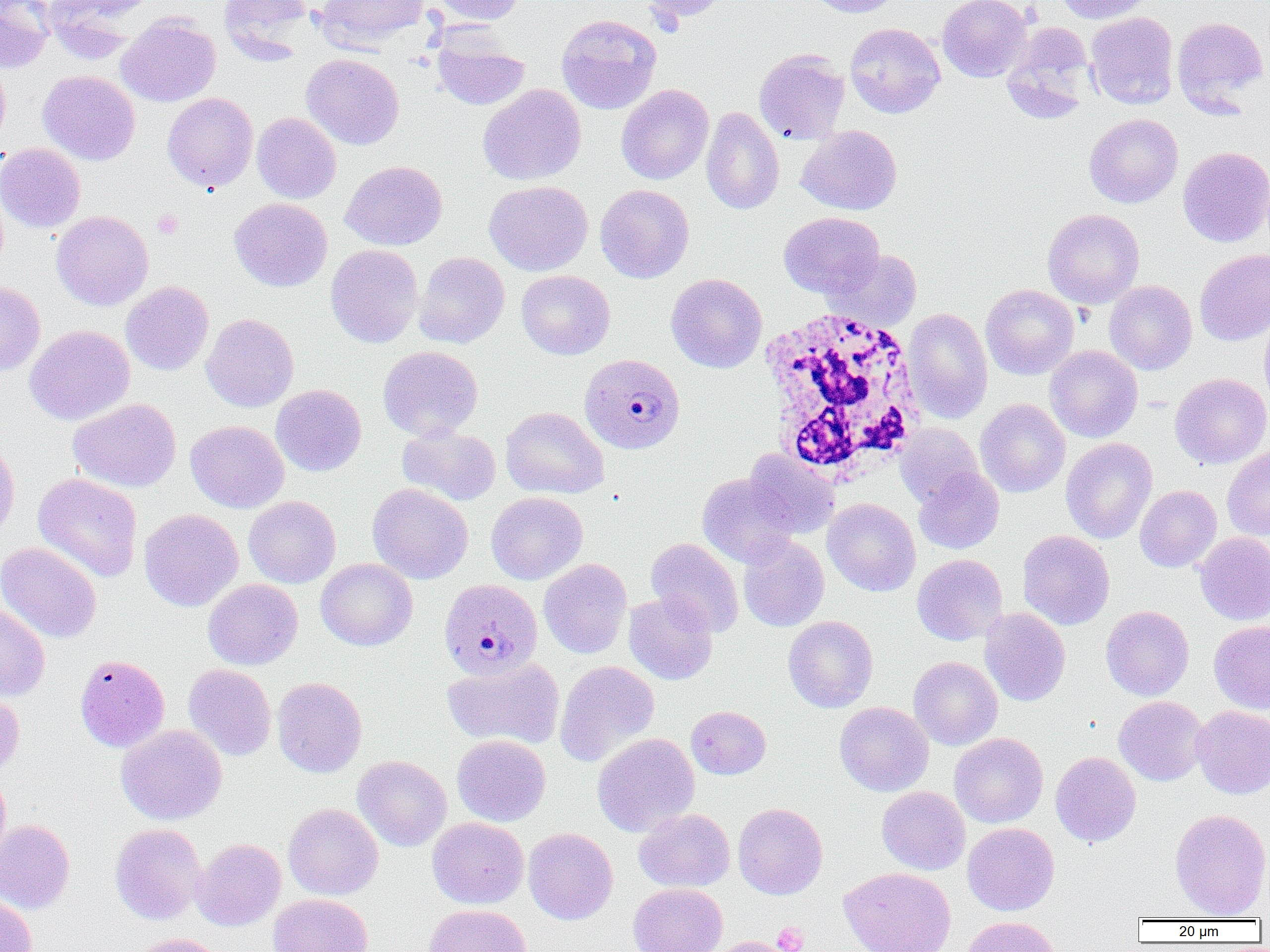
Summary:
  - Coordinate format: approximate bounding boxes as named x1/y1/x2/y2 corners in pixels
  - White blood cell locations: (x1=757, y1=308, x2=928, y2=479)
  - Plasmodium malariae-infected red blood cell locations: (x1=580, y1=353, x2=686, y2=455), (x1=441, y1=583, x2=544, y2=684)
  - Uninfected red blood cell locations: (x1=0, y1=0, x2=55, y2=73), (x1=42, y1=0, x2=148, y2=62), (x1=219, y1=0, x2=312, y2=62), (x1=314, y1=0, x2=428, y2=52), (x1=431, y1=0, x2=526, y2=25), (x1=641, y1=0, x2=730, y2=24), (x1=806, y1=0, x2=902, y2=17), (x1=937, y1=0, x2=1032, y2=82), (x1=1055, y1=0, x2=1151, y2=24), (x1=1085, y1=12, x2=1178, y2=109), (x1=556, y1=13, x2=662, y2=114), (x1=116, y1=14, x2=220, y2=107), (x1=1172, y1=16, x2=1268, y2=112), (x1=844, y1=23, x2=945, y2=118), (x1=1002, y1=23, x2=1095, y2=123), (x1=432, y1=31, x2=529, y2=110), (x1=754, y1=49, x2=850, y2=144), (x1=301, y1=53, x2=404, y2=150), (x1=0, y1=56, x2=11, y2=149), (x1=37, y1=70, x2=140, y2=165), (x1=478, y1=84, x2=586, y2=186), (x1=616, y1=84, x2=714, y2=184), (x1=162, y1=93, x2=258, y2=191), (x1=701, y1=106, x2=784, y2=215), (x1=252, y1=112, x2=341, y2=204), (x1=1084, y1=113, x2=1183, y2=207), (x1=796, y1=125, x2=902, y2=215), (x1=0, y1=143, x2=86, y2=232), (x1=1178, y1=146, x2=1270, y2=247), (x1=340, y1=160, x2=447, y2=250), (x1=484, y1=180, x2=593, y2=276), (x1=595, y1=184, x2=694, y2=283), (x1=229, y1=198, x2=332, y2=291), (x1=1043, y1=208, x2=1144, y2=308), (x1=52, y1=211, x2=153, y2=310), (x1=778, y1=211, x2=884, y2=297), (x1=326, y1=244, x2=423, y2=347), (x1=1195, y1=248, x2=1270, y2=346), (x1=825, y1=249, x2=923, y2=330), (x1=413, y1=252, x2=509, y2=348), (x1=516, y1=270, x2=615, y2=360), (x1=666, y1=273, x2=767, y2=373), (x1=0, y1=280, x2=46, y2=376), (x1=1104, y1=280, x2=1197, y2=375), (x1=121, y1=281, x2=214, y2=375), (x1=981, y1=285, x2=1078, y2=379), (x1=903, y1=308, x2=993, y2=423), (x1=1259, y1=312, x2=1270, y2=410), (x1=201, y1=313, x2=299, y2=412), (x1=25, y1=325, x2=135, y2=425), (x1=378, y1=345, x2=483, y2=440), (x1=1045, y1=345, x2=1143, y2=442), (x1=1169, y1=373, x2=1270, y2=468), (x1=271, y1=384, x2=366, y2=476), (x1=68, y1=398, x2=181, y2=492), (x1=974, y1=399, x2=1070, y2=497), (x1=501, y1=406, x2=608, y2=499), (x1=185, y1=420, x2=289, y2=513), (x1=397, y1=423, x2=501, y2=505), (x1=895, y1=423, x2=983, y2=507), (x1=0, y1=437, x2=19, y2=542), (x1=1060, y1=438, x2=1157, y2=544), (x1=1222, y1=446, x2=1270, y2=540), (x1=744, y1=450, x2=841, y2=538), (x1=914, y1=467, x2=1004, y2=553), (x1=33, y1=473, x2=143, y2=582), (x1=697, y1=473, x2=799, y2=568), (x1=368, y1=482, x2=473, y2=584), (x1=1135, y1=485, x2=1221, y2=572), (x1=486, y1=492, x2=587, y2=584), (x1=243, y1=496, x2=341, y2=588), (x1=822, y1=498, x2=920, y2=597), (x1=139, y1=508, x2=243, y2=611), (x1=1018, y1=530, x2=1115, y2=630), (x1=1194, y1=532, x2=1270, y2=625), (x1=738, y1=535, x2=829, y2=631), (x1=646, y1=538, x2=745, y2=637), (x1=0, y1=541, x2=102, y2=643), (x1=912, y1=554, x2=1008, y2=645), (x1=316, y1=558, x2=418, y2=650), (x1=539, y1=558, x2=632, y2=659), (x1=203, y1=579, x2=303, y2=670), (x1=623, y1=591, x2=718, y2=685), (x1=0, y1=601, x2=50, y2=700), (x1=1101, y1=605, x2=1194, y2=700), (x1=980, y1=607, x2=1070, y2=706), (x1=783, y1=615, x2=879, y2=713), (x1=1209, y1=621, x2=1270, y2=714), (x1=75, y1=654, x2=170, y2=752), (x1=442, y1=656, x2=565, y2=750), (x1=908, y1=656, x2=1003, y2=750), (x1=555, y1=660, x2=660, y2=767), (x1=183, y1=664, x2=276, y2=760), (x1=272, y1=677, x2=367, y2=777), (x1=0, y1=688, x2=25, y2=779), (x1=1114, y1=696, x2=1209, y2=786), (x1=834, y1=702, x2=934, y2=796), (x1=1191, y1=705, x2=1270, y2=798), (x1=686, y1=706, x2=771, y2=780), (x1=116, y1=724, x2=227, y2=825), (x1=592, y1=733, x2=699, y2=837), (x1=949, y1=733, x2=1048, y2=827), (x1=452, y1=734, x2=551, y2=826), (x1=1050, y1=751, x2=1141, y2=847), (x1=353, y1=755, x2=452, y2=851), (x1=0, y1=771, x2=11, y2=869), (x1=876, y1=786, x2=970, y2=875), (x1=283, y1=802, x2=383, y2=900), (x1=733, y1=802, x2=828, y2=899), (x1=634, y1=808, x2=735, y2=892), (x1=1169, y1=808, x2=1270, y2=918), (x1=427, y1=817, x2=529, y2=909), (x1=0, y1=819, x2=76, y2=913), (x1=962, y1=822, x2=1059, y2=915), (x1=110, y1=823, x2=207, y2=925), (x1=523, y1=828, x2=618, y2=924), (x1=192, y1=838, x2=286, y2=931), (x1=839, y1=866, x2=956, y2=952), (x1=629, y1=883, x2=727, y2=952), (x1=268, y1=893, x2=373, y2=952), (x1=0, y1=896, x2=37, y2=952), (x1=424, y1=904, x2=532, y2=952), (x1=961, y1=915, x2=1060, y2=952), (x1=124, y1=933, x2=230, y2=952), (x1=705, y1=936, x2=795, y2=952)
  - Platelet locations: (x1=152, y1=209, x2=183, y2=238), (x1=772, y1=924, x2=808, y2=952)
  - Slide-level diagnosis: Plasmodium malariae
  - Magnification: 1000x
  - Modality: optical microscopy
  - Preparation: thin blood smear
  - Field of view: single
  - Image size: 1270×952 pixels